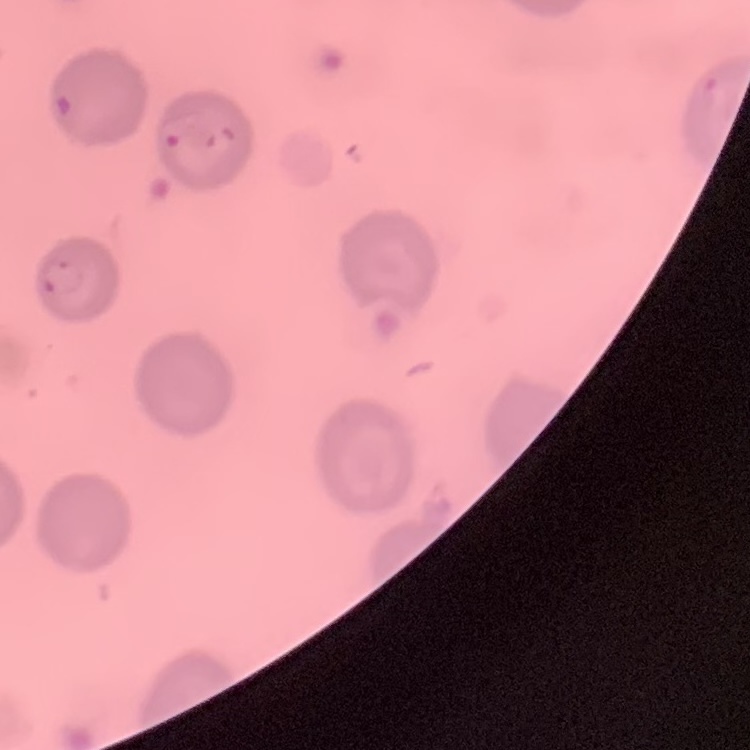
Summary:
  - Erythrocyte morphology: no rouleaux formation
  - Image type: one tile cut from a larger photomicrograph
  - Preparation: thin peripheral smear
  - Stain: Field's or Giemsa